Identify the parasite.
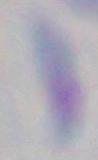

Toxoplasma gondii.

magnification: 1000x
modality: photomicrograph